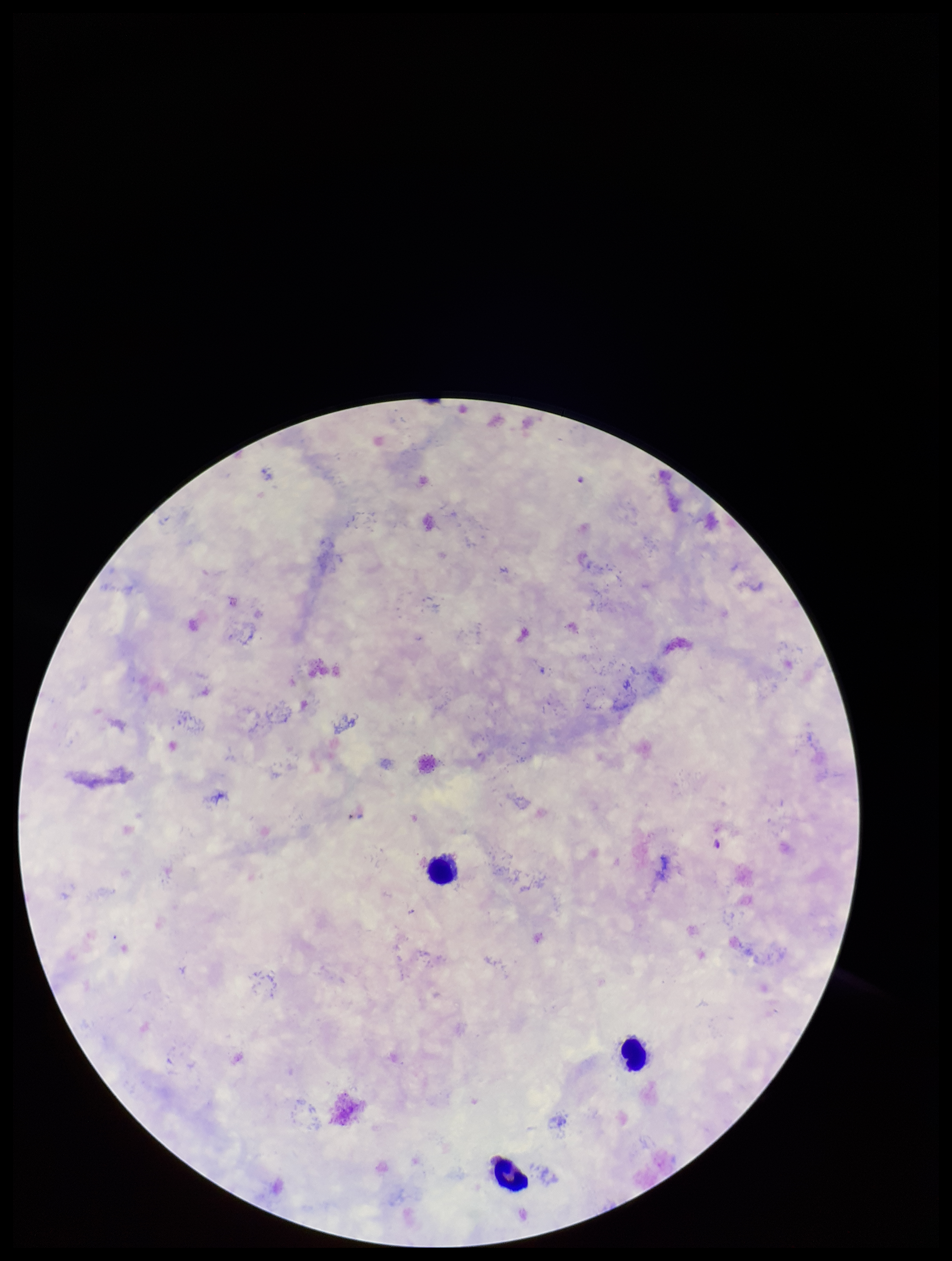
Plasmodium parasites: none detected. Species reported for this patient: Plasmodium falciparum. Stained with Giemsa. Smartphone photograph taken through the eyepiece of a microscope. Patient malaria status: infected. Image is 952×1261 pixels. Parasite count: 0. One field from this slide. Preparation: thick smear. Leukocyte count: 3.